Classify this cell by malaria status.
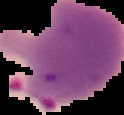
It is parasitized.

{
  "image_type": "cell region segmented out of the field of view; surrounding area masked to black",
  "preparation": "thin blood film",
  "image_size": "124×115 pixels"
}